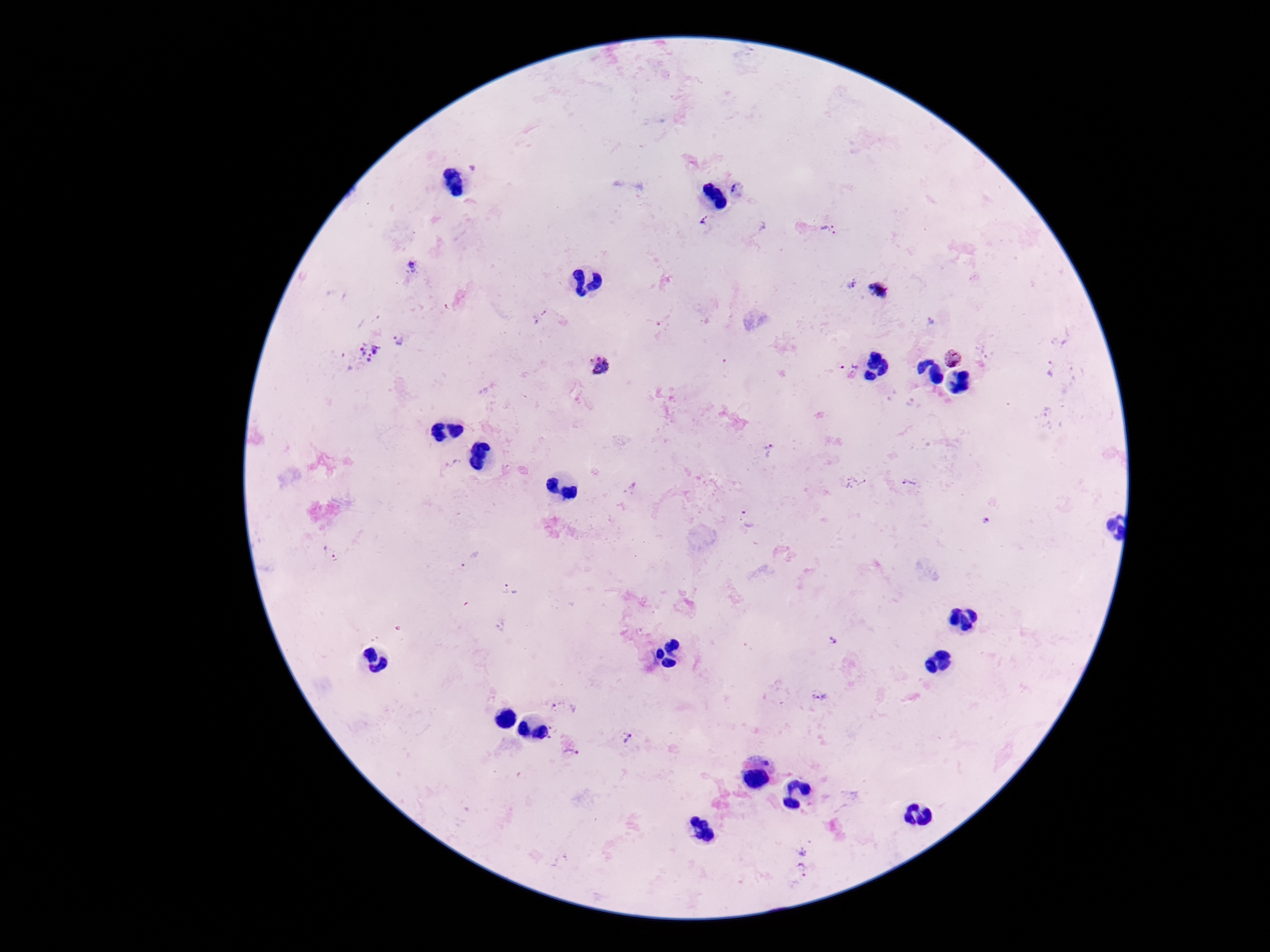

Approximate object centers, in pixels from the top-left corner.
Summary:
  - Plasmodium parasite locations: (x=737, y=189), (x=702, y=221), (x=829, y=230), (x=411, y=268), (x=849, y=284), (x=881, y=291), (x=545, y=313), (x=535, y=322), (x=931, y=322), (x=400, y=341), (x=362, y=354), (x=952, y=357), (x=599, y=365), (x=849, y=366), (x=1053, y=370), (x=769, y=450), (x=855, y=482), (x=909, y=482), (x=747, y=520), (x=331, y=554), (x=470, y=558), (x=508, y=589), (x=833, y=642), (x=821, y=697), (x=563, y=705), (x=553, y=729), (x=626, y=739), (x=571, y=753), (x=803, y=851), (x=803, y=870)
  - Magnification: 100x
  - Patient malaria status: positive
  - Capture: smartphone camera through the microscope eyepiece
  - Stain: Giemsa
  - Image size: 1270×952 pixels
  - Field of view: single
  - Preparation: thick peripheral-blood smear